Comment on the morphology of the erythrocytes.
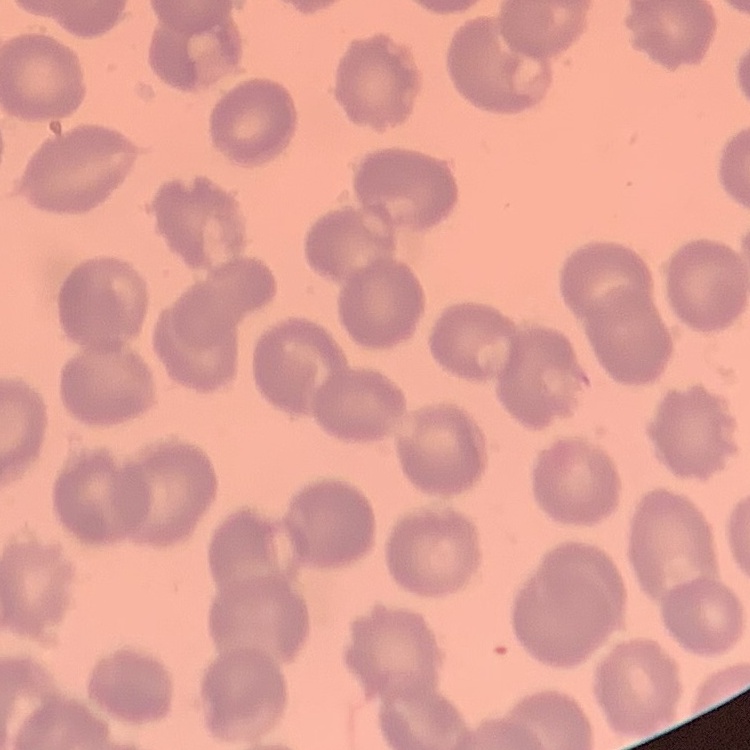

They show no rouleaux formation.

Square crop of a larger photomicrograph. Field's or Giemsa stain. Thin peripheral smear.